Name the parasite shown.
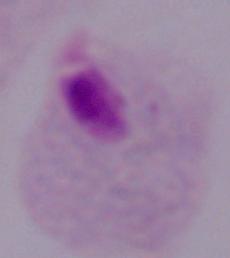

A trichomonad.

Summary:
  - Magnification: 1000x
  - Modality: micrograph